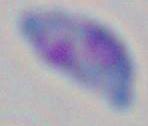

Toxoplasma gondii is shown. Captured at 1000x magnification. Photomicrograph.